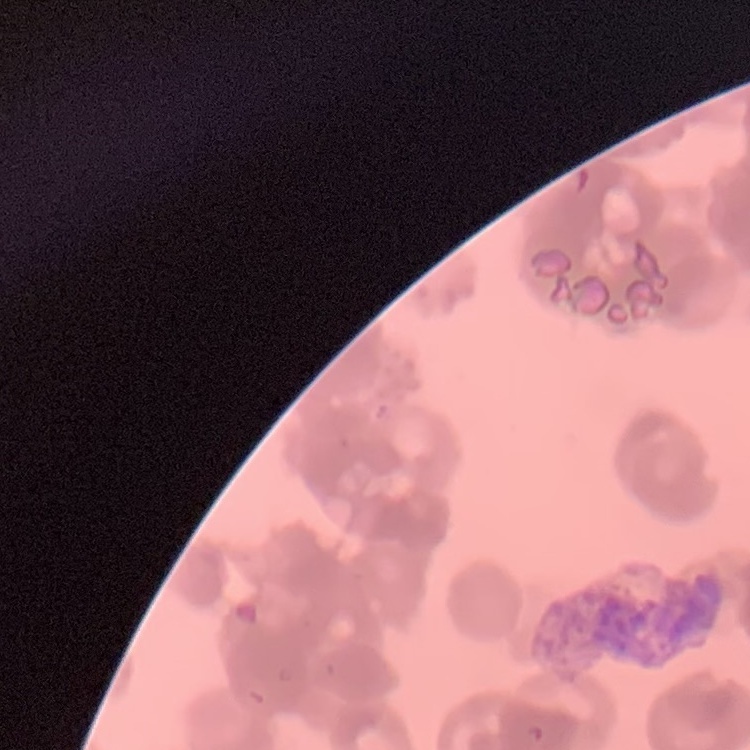

Summary:
  - Red blood cell morphology: rouleaux formation
  - Image type: square crop of a larger photomicrograph
  - Stain: Field's or Giemsa
  - Preparation: thin blood smear